Give the extent of all uninfected red blood cells.
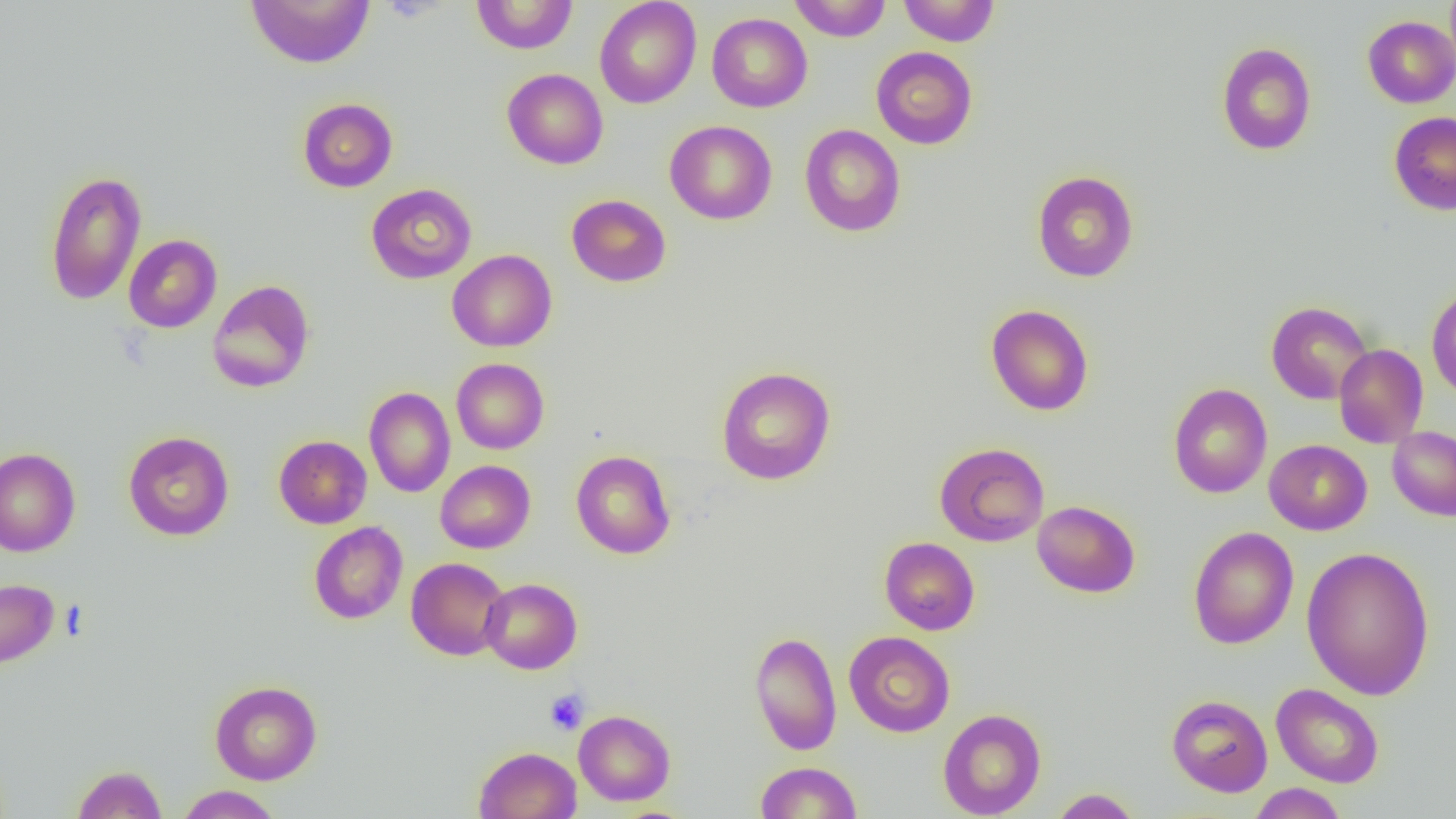

Approximate bounding boxes as named x1/y1/x2/y2 corners in pixels.
Uninfected red blood cells: (x1=245, y1=0, x2=375, y2=69), (x1=471, y1=0, x2=579, y2=54), (x1=594, y1=0, x2=701, y2=108), (x1=790, y1=0, x2=891, y2=41), (x1=899, y1=0, x2=999, y2=46), (x1=1444, y1=0, x2=1456, y2=73), (x1=707, y1=13, x2=812, y2=112), (x1=1362, y1=15, x2=1456, y2=108), (x1=1216, y1=42, x2=1317, y2=155), (x1=871, y1=46, x2=978, y2=149), (x1=501, y1=68, x2=608, y2=169), (x1=297, y1=97, x2=398, y2=192), (x1=1388, y1=111, x2=1456, y2=215), (x1=664, y1=120, x2=777, y2=224), (x1=799, y1=124, x2=906, y2=237), (x1=44, y1=170, x2=147, y2=306), (x1=1032, y1=170, x2=1139, y2=282), (x1=365, y1=183, x2=477, y2=284), (x1=567, y1=194, x2=671, y2=287), (x1=124, y1=234, x2=222, y2=333), (x1=447, y1=249, x2=557, y2=352), (x1=207, y1=280, x2=315, y2=393), (x1=1426, y1=285, x2=1456, y2=400), (x1=1265, y1=301, x2=1373, y2=404), (x1=985, y1=304, x2=1094, y2=416), (x1=1333, y1=344, x2=1428, y2=448), (x1=451, y1=358, x2=549, y2=454), (x1=716, y1=367, x2=836, y2=485), (x1=1168, y1=383, x2=1272, y2=499), (x1=364, y1=386, x2=455, y2=498), (x1=1387, y1=426, x2=1456, y2=521), (x1=123, y1=431, x2=234, y2=540), (x1=274, y1=435, x2=372, y2=529), (x1=1264, y1=439, x2=1372, y2=535), (x1=935, y1=442, x2=1049, y2=547), (x1=0, y1=447, x2=81, y2=557), (x1=571, y1=450, x2=676, y2=559), (x1=435, y1=460, x2=535, y2=553), (x1=1032, y1=500, x2=1140, y2=597), (x1=309, y1=522, x2=407, y2=624), (x1=1187, y1=526, x2=1299, y2=649), (x1=879, y1=537, x2=979, y2=635), (x1=1301, y1=546, x2=1435, y2=700), (x1=406, y1=557, x2=510, y2=660), (x1=0, y1=578, x2=59, y2=669), (x1=480, y1=578, x2=582, y2=674), (x1=749, y1=631, x2=842, y2=755), (x1=844, y1=631, x2=955, y2=737), (x1=210, y1=679, x2=322, y2=785), (x1=1271, y1=683, x2=1384, y2=788), (x1=1166, y1=694, x2=1272, y2=797), (x1=938, y1=708, x2=1046, y2=818), (x1=574, y1=710, x2=675, y2=806), (x1=474, y1=746, x2=581, y2=818), (x1=755, y1=761, x2=862, y2=818), (x1=72, y1=765, x2=167, y2=819), (x1=1247, y1=783, x2=1348, y2=818), (x1=176, y1=785, x2=283, y2=818), (x1=1048, y1=788, x2=1143, y2=818).

Summary:
  - Platelet locations: (x1=544, y1=688, x2=589, y2=735)
  - Slide-level diagnosis: negative for blood parasites
  - Image size: 1456×819 pixels
  - Magnification: 1000x
  - Modality: optical microscopy
  - Field of view: single
  - Preparation: thin blood smear